Locate every malaria parasite.
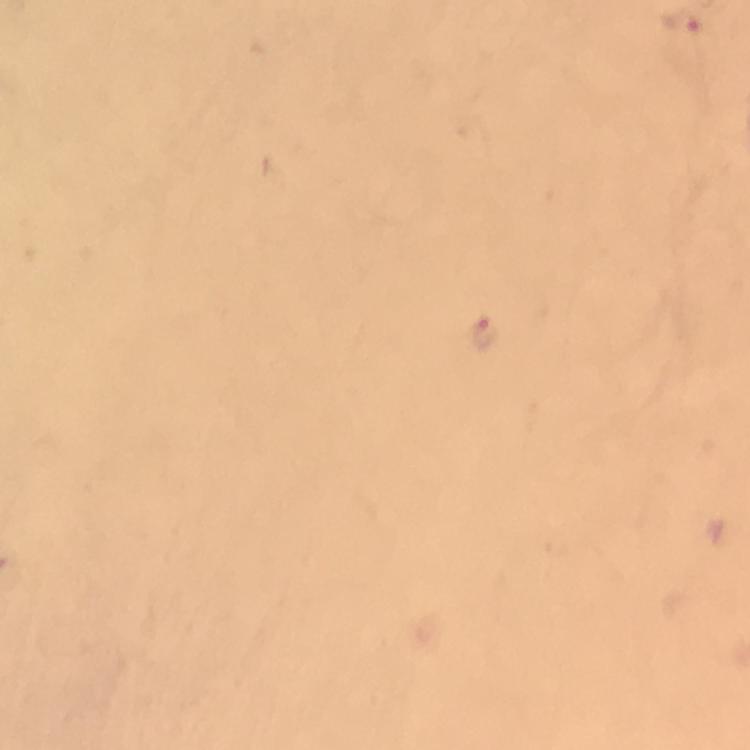

Approximate centers as [x, y] in pixels.
Malaria parasites: [679, 22], [483, 332].

immersion_oil: used
cropped_from: one field of view
stain: Giemsa
magnification: 100x
image_size: 750×750 pixels
preparation: thick blood film
capture: smartphone photograph through a microscope
context: from a malaria diagnostic workup